Give the extent of all Plasmodium vivax-infected red blood cells.
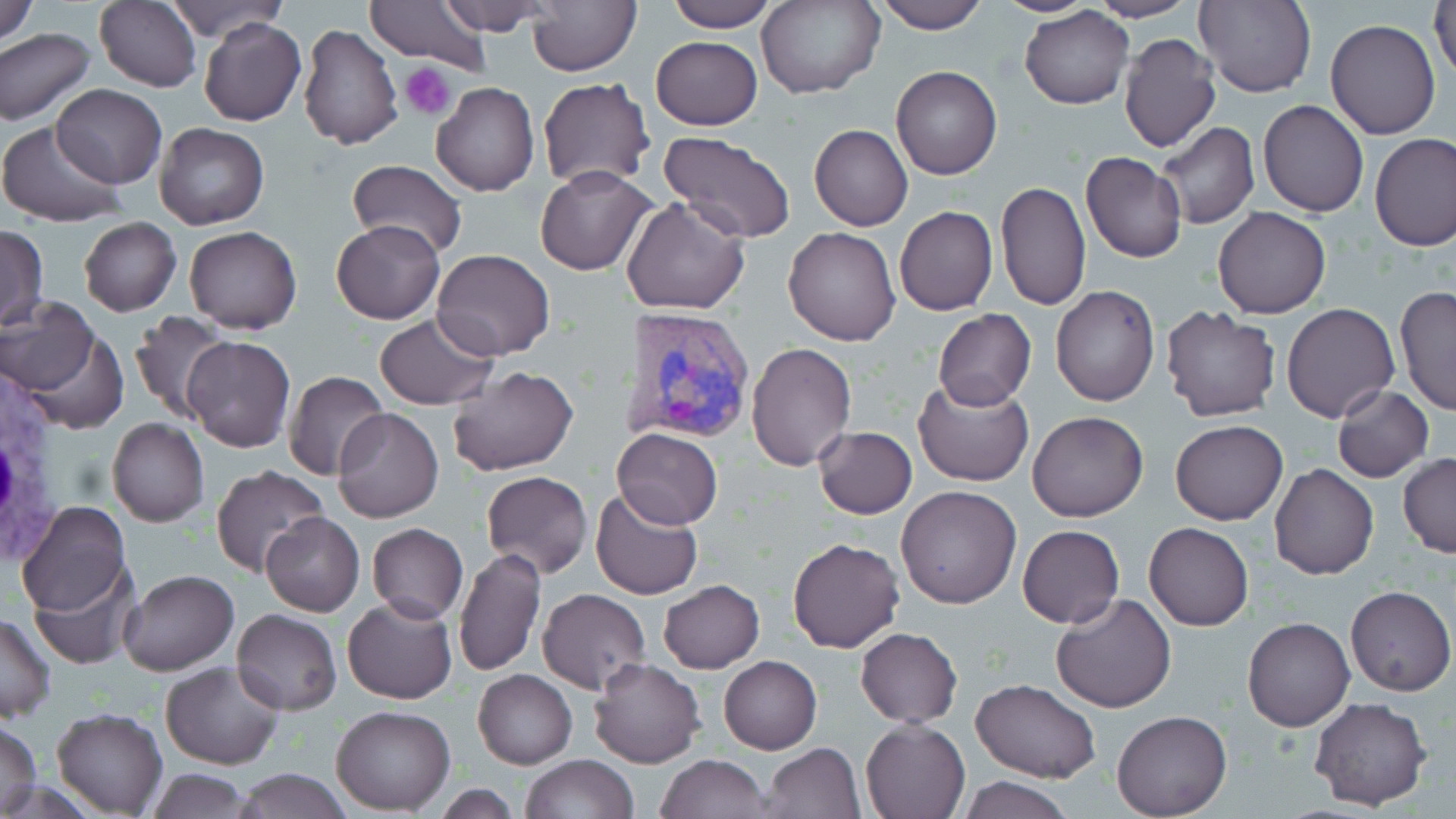

Approximate bounding boxes as named x1/y1/x2/y2 corners in pixels.
Plasmodium vivax-infected red blood cells: (x1=617, y1=306, x2=756, y2=448).

slide-level diagnosis = Plasmodium vivax
stain = May-Grünwald-Giemsa
white blood cell locations = approximate bounding boxes as named x1/y1/x2/y2 corners in pixels: (x1=0, y1=359, x2=84, y2=578)
modality = optical microscopy
preparation = thin blood smear
magnification = 1000x
platelet locations = approximate bounding boxes as named x1/y1/x2/y2 corners in pixels: (x1=402, y1=63, x2=457, y2=119)
uninfected red blood cell locations = approximate bounding boxes as named x1/y1/x2/y2 corners in pixels: (x1=0, y1=0, x2=38, y2=48), (x1=95, y1=0, x2=202, y2=91), (x1=164, y1=0, x2=287, y2=45), (x1=365, y1=0, x2=493, y2=70), (x1=436, y1=0, x2=559, y2=35), (x1=527, y1=0, x2=641, y2=76), (x1=663, y1=0, x2=779, y2=32), (x1=875, y1=0, x2=988, y2=34), (x1=988, y1=0, x2=1106, y2=16), (x1=1089, y1=0, x2=1197, y2=22), (x1=1195, y1=0, x2=1315, y2=97), (x1=1430, y1=0, x2=1456, y2=87), (x1=760, y1=1, x2=882, y2=99), (x1=1019, y1=7, x2=1134, y2=109), (x1=199, y1=15, x2=307, y2=126), (x1=1324, y1=20, x2=1442, y2=139), (x1=297, y1=22, x2=404, y2=150), (x1=0, y1=29, x2=98, y2=126), (x1=1118, y1=33, x2=1221, y2=153), (x1=650, y1=36, x2=763, y2=129), (x1=891, y1=65, x2=1001, y2=180), (x1=537, y1=77, x2=655, y2=190), (x1=52, y1=83, x2=166, y2=188), (x1=430, y1=83, x2=539, y2=197), (x1=1259, y1=100, x2=1369, y2=217), (x1=0, y1=119, x2=128, y2=227), (x1=1156, y1=121, x2=1259, y2=230), (x1=154, y1=123, x2=270, y2=230), (x1=809, y1=124, x2=913, y2=231), (x1=660, y1=130, x2=797, y2=246), (x1=1370, y1=133, x2=1456, y2=251), (x1=1081, y1=151, x2=1185, y2=263), (x1=346, y1=160, x2=469, y2=259), (x1=535, y1=167, x2=657, y2=275), (x1=996, y1=181, x2=1091, y2=314), (x1=620, y1=196, x2=750, y2=316), (x1=894, y1=206, x2=997, y2=315), (x1=1211, y1=206, x2=1331, y2=318), (x1=79, y1=217, x2=181, y2=315), (x1=331, y1=220, x2=445, y2=324), (x1=184, y1=224, x2=302, y2=335), (x1=0, y1=226, x2=48, y2=330), (x1=784, y1=227, x2=900, y2=346), (x1=431, y1=249, x2=555, y2=360), (x1=1394, y1=283, x2=1456, y2=417), (x1=1051, y1=285, x2=1159, y2=406), (x1=1, y1=296, x2=100, y2=398), (x1=1282, y1=303, x2=1400, y2=422), (x1=1159, y1=305, x2=1283, y2=424), (x1=128, y1=309, x2=235, y2=423), (x1=932, y1=310, x2=1036, y2=410), (x1=373, y1=314, x2=497, y2=411), (x1=15, y1=322, x2=128, y2=434), (x1=183, y1=335, x2=295, y2=452), (x1=745, y1=342, x2=857, y2=471), (x1=446, y1=365, x2=580, y2=477), (x1=283, y1=372, x2=391, y2=480), (x1=912, y1=376, x2=1036, y2=489), (x1=1331, y1=385, x2=1433, y2=482), (x1=331, y1=407, x2=444, y2=525), (x1=1027, y1=411, x2=1149, y2=523), (x1=108, y1=418, x2=209, y2=527), (x1=1169, y1=419, x2=1288, y2=525), (x1=813, y1=426, x2=917, y2=518), (x1=611, y1=427, x2=723, y2=529), (x1=1398, y1=453, x2=1456, y2=558), (x1=1268, y1=464, x2=1379, y2=581), (x1=211, y1=465, x2=327, y2=576), (x1=481, y1=471, x2=593, y2=578), (x1=894, y1=485, x2=1020, y2=610), (x1=590, y1=488, x2=703, y2=601), (x1=17, y1=498, x2=131, y2=617), (x1=261, y1=512, x2=364, y2=615), (x1=1144, y1=521, x2=1253, y2=631), (x1=367, y1=523, x2=469, y2=622), (x1=1017, y1=525, x2=1125, y2=629), (x1=788, y1=538, x2=904, y2=653), (x1=455, y1=548, x2=546, y2=679), (x1=30, y1=561, x2=140, y2=669), (x1=117, y1=570, x2=237, y2=677), (x1=659, y1=580, x2=765, y2=673), (x1=1345, y1=585, x2=1455, y2=697), (x1=537, y1=588, x2=649, y2=694), (x1=1050, y1=592, x2=1177, y2=713), (x1=341, y1=596, x2=456, y2=704), (x1=232, y1=609, x2=342, y2=714), (x1=0, y1=614, x2=55, y2=723), (x1=1242, y1=617, x2=1354, y2=732), (x1=856, y1=627, x2=962, y2=726), (x1=718, y1=655, x2=821, y2=755), (x1=589, y1=657, x2=707, y2=769), (x1=160, y1=661, x2=285, y2=769), (x1=473, y1=669, x2=578, y2=769), (x1=972, y1=678, x2=1099, y2=784), (x1=1309, y1=697, x2=1432, y2=810), (x1=332, y1=706, x2=456, y2=814), (x1=52, y1=708, x2=167, y2=817), (x1=1112, y1=709, x2=1232, y2=818), (x1=861, y1=717, x2=970, y2=819), (x1=0, y1=720, x2=42, y2=817), (x1=760, y1=742, x2=866, y2=818), (x1=655, y1=753, x2=772, y2=818), (x1=520, y1=754, x2=639, y2=819), (x1=146, y1=767, x2=254, y2=819), (x1=230, y1=768, x2=353, y2=819), (x1=955, y1=776, x2=1076, y2=818)
field of view = single
image size = 1456×819 pixels